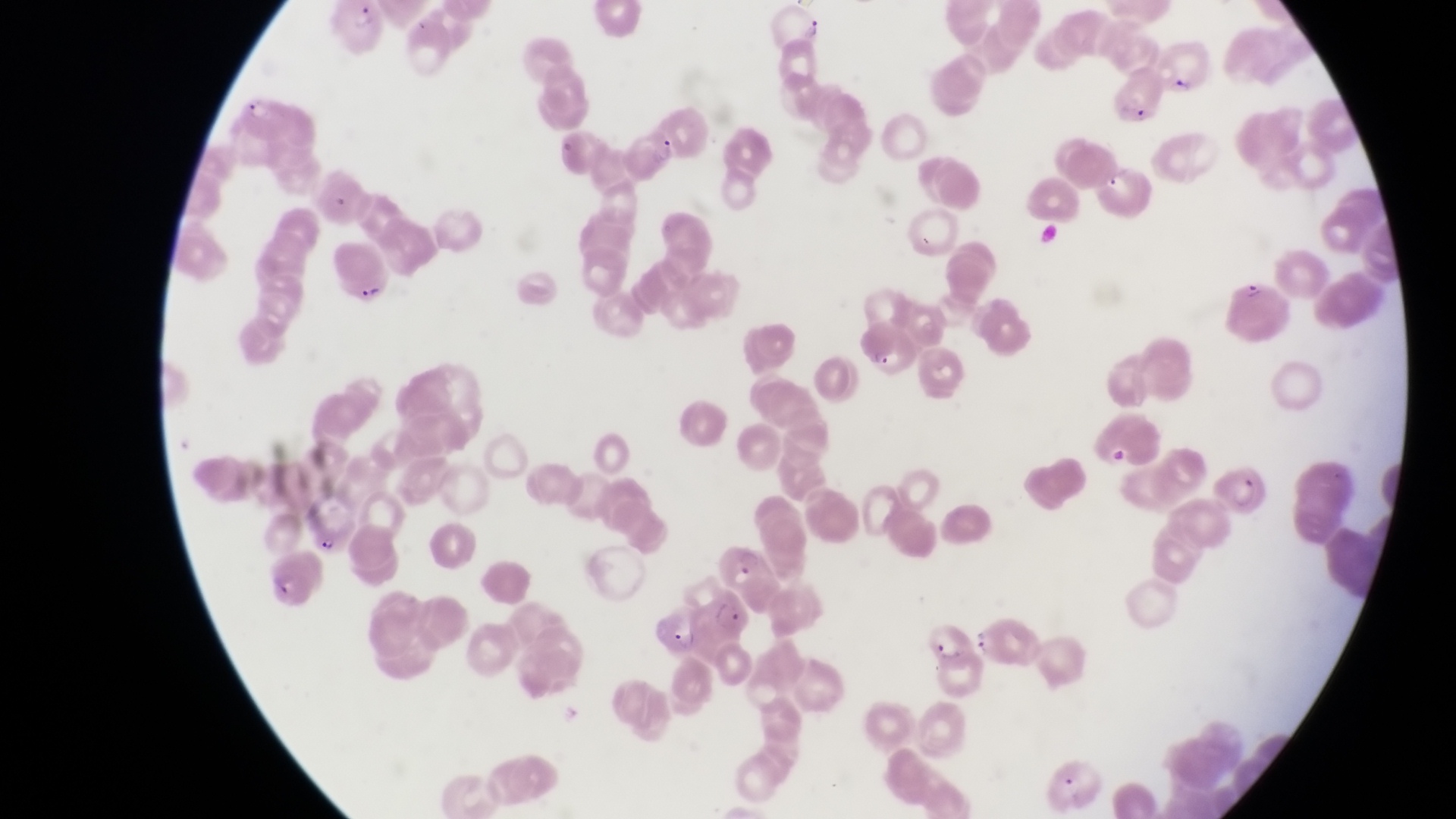

Approximate bounding boxes as [left, top, right, bottom] in pixels.
Summary:
  - Parasitised red blood cell locations: [328, 3, 391, 59], [769, 13, 827, 49], [1156, 40, 1214, 104], [1105, 71, 1164, 129], [240, 92, 307, 148], [620, 132, 689, 184], [330, 248, 399, 307], [1225, 277, 1294, 343], [851, 327, 918, 379], [1084, 422, 1161, 475], [1213, 465, 1268, 517], [303, 497, 356, 556], [714, 544, 787, 603], [261, 551, 333, 611], [658, 602, 707, 654], [925, 626, 984, 675], [1043, 756, 1106, 812]
  - Field of view: single
  - Image size: 1456×819 pixels
  - Country: Uganda
  - Magnification: 1000x
  - Capture: smartphone photograph through the eyepiece of an Olympus CX-23 microscope
  - Preparation: thin blood film